State the blood parasite species.
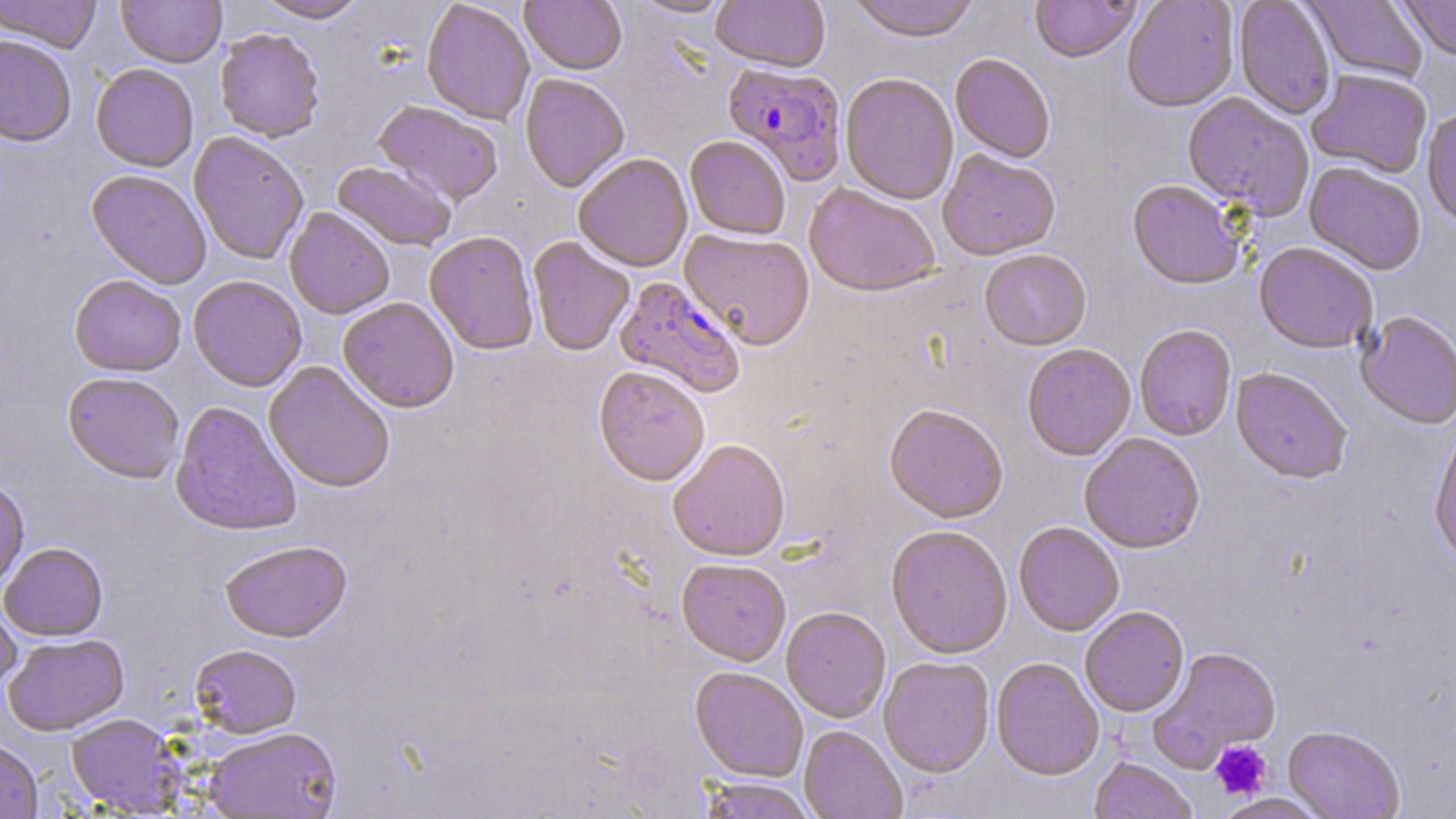
Plasmodium falciparum.

field of view = one of a larger specimen
magnification = 1000x
uninfected red blood cell locations = approximate bounding boxes as (x1,y1)-(x2,y2) corner pairs in pixels: (0,0)-(102,53), (117,0)-(226,68), (253,0)-(369,23), (520,0)-(627,77), (631,0)-(733,19), (710,0)-(830,75), (847,0)-(980,45), (1030,0)-(1141,65), (1122,0)-(1239,114), (1302,0)-(1430,85), (1397,0)-(1456,63), (1233,1)-(1336,120), (421,2)-(535,126), (214,30)-(325,143), (0,35)-(77,147), (950,55)-(1055,165), (91,63)-(199,172), (1307,70)-(1432,179), (519,75)-(630,194), (840,75)-(958,206), (1182,94)-(1313,220), (373,101)-(502,208), (1421,108)-(1456,230), (189,132)-(308,265), (685,138)-(791,241), (938,151)-(1060,262), (573,155)-(693,274), (332,162)-(456,253), (1304,164)-(1426,276), (85,170)-(211,289), (1127,182)-(1244,292), (803,185)-(940,299), (284,208)-(394,320), (679,230)-(815,351), (425,233)-(538,356), (528,238)-(634,356), (1253,243)-(1377,356), (979,251)-(1091,352), (69,275)-(186,377), (188,276)-(307,393), (338,298)-(459,415), (1355,313)-(1456,430), (1134,326)-(1237,442), (1022,345)-(1136,462), (263,361)-(395,494), (593,368)-(710,489), (1230,369)-(1352,486), (62,373)-(185,486), (169,402)-(302,537), (884,406)-(1008,524), (1428,426)-(1456,568), (1079,434)-(1205,555), (667,441)-(791,563), (0,480)-(30,593), (1014,523)-(1124,637), (886,527)-(1012,660), (219,542)-(353,644), (0,543)-(108,641), (676,560)-(791,668), (0,596)-(22,697), (781,608)-(891,724), (1080,608)-(1189,718), (3,634)-(130,737), (190,645)-(301,739), (1147,648)-(1282,773), (879,658)-(995,778), (991,659)-(1104,781), (690,668)-(807,782), (65,714)-(185,815), (799,726)-(907,819), (1283,728)-(1404,819), (204,729)-(342,818), (0,739)-(43,818), (1089,758)-(1197,819), (699,778)-(816,819), (1214,794)-(1331,819)
image size = 1456×819 pixels
preparation = thin blood film
Plasmodium falciparum-infected red blood cell locations = approximate bounding boxes as (x1,y1)-(x2,y2) corner pairs in pixels: (722,63)-(847,186), (614,277)-(746,399)
platelet locations = approximate bounding boxes as (x1,y1)-(x2,y2) corner pairs in pixels: (1210,740)-(1273,800)
modality = optical microscopy
stain = May-Grünwald-Giemsa